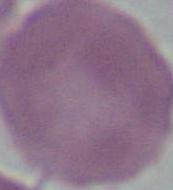
magnification = 1000x
identification = erythrocyte
modality = micrograph